Comment on the morphology of the red blood cells.
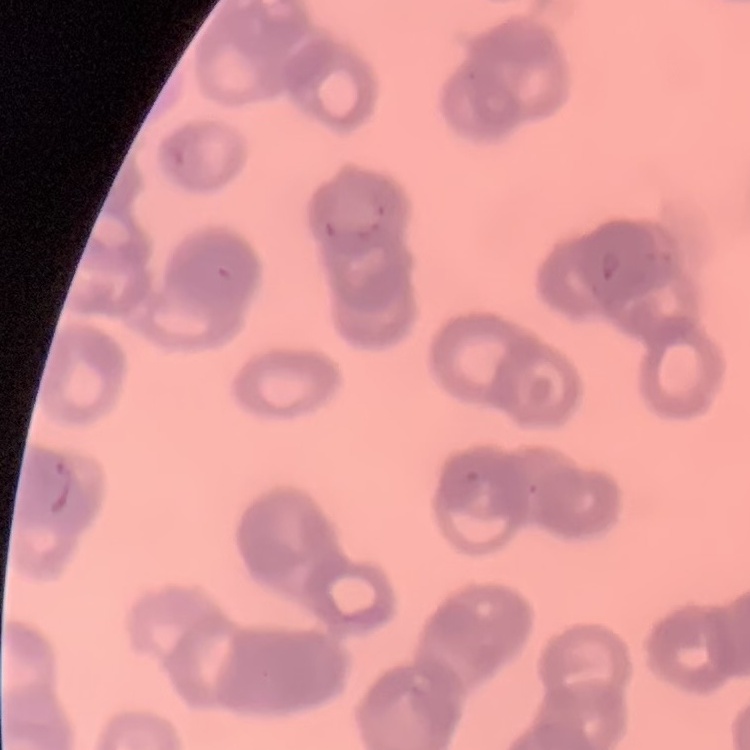
Rouleaux formation.

preparation = thin blood film
image type = one tile cut from a larger photomicrograph
stain = Field's or Giemsa